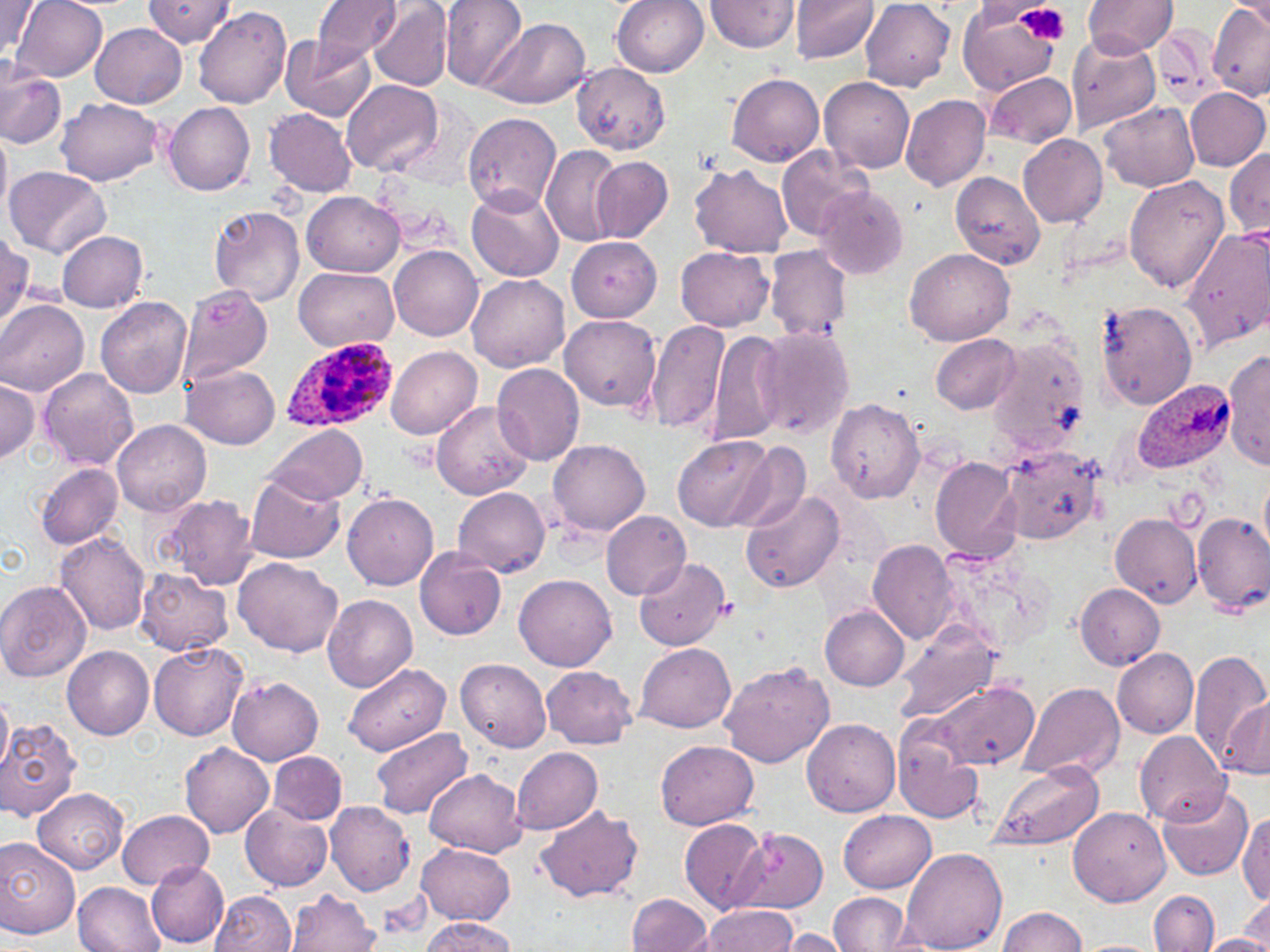

Summary:
  - Coordinate format: approximate bounding boxes as named x1/y1/x2/y2 corners in pixels
  - Uninfected red blood cell locations: (x1=12, y1=0, x2=108, y2=82), (x1=144, y1=0, x2=236, y2=46), (x1=312, y1=0, x2=403, y2=61), (x1=369, y1=0, x2=454, y2=92), (x1=441, y1=0, x2=529, y2=92), (x1=613, y1=0, x2=709, y2=77), (x1=705, y1=0, x2=799, y2=55), (x1=789, y1=0, x2=879, y2=65), (x1=1083, y1=1, x2=1176, y2=57), (x1=860, y1=2, x2=954, y2=90), (x1=1, y1=3, x2=40, y2=60), (x1=1207, y1=4, x2=1270, y2=100), (x1=958, y1=5, x2=1062, y2=95), (x1=194, y1=7, x2=292, y2=108), (x1=482, y1=18, x2=591, y2=109), (x1=90, y1=23, x2=186, y2=108), (x1=1154, y1=27, x2=1223, y2=106), (x1=280, y1=34, x2=377, y2=121), (x1=1068, y1=34, x2=1160, y2=131), (x1=572, y1=63, x2=670, y2=153), (x1=0, y1=69, x2=67, y2=150), (x1=984, y1=72, x2=1077, y2=147), (x1=725, y1=73, x2=824, y2=166), (x1=819, y1=77, x2=914, y2=173), (x1=342, y1=79, x2=444, y2=176), (x1=1185, y1=87, x2=1269, y2=171), (x1=900, y1=92, x2=990, y2=191), (x1=56, y1=98, x2=163, y2=186), (x1=162, y1=102, x2=256, y2=197), (x1=1100, y1=102, x2=1199, y2=193), (x1=265, y1=109, x2=358, y2=196), (x1=461, y1=111, x2=563, y2=214), (x1=0, y1=125, x2=11, y2=224), (x1=1017, y1=132, x2=1107, y2=227), (x1=541, y1=146, x2=626, y2=246), (x1=777, y1=146, x2=872, y2=242), (x1=1224, y1=151, x2=1270, y2=236), (x1=590, y1=156, x2=674, y2=242), (x1=691, y1=164, x2=793, y2=258), (x1=4, y1=166, x2=111, y2=259), (x1=950, y1=172, x2=1045, y2=269), (x1=1124, y1=173, x2=1229, y2=292), (x1=468, y1=184, x2=565, y2=280), (x1=815, y1=187, x2=909, y2=279), (x1=303, y1=191, x2=403, y2=277), (x1=207, y1=204, x2=306, y2=307), (x1=1178, y1=225, x2=1270, y2=354), (x1=0, y1=231, x2=32, y2=324), (x1=57, y1=231, x2=148, y2=311), (x1=567, y1=236, x2=661, y2=322), (x1=391, y1=245, x2=484, y2=340), (x1=904, y1=246, x2=1016, y2=345), (x1=765, y1=247, x2=851, y2=341), (x1=676, y1=248, x2=774, y2=332), (x1=293, y1=267, x2=399, y2=350), (x1=467, y1=274, x2=568, y2=371), (x1=177, y1=281, x2=273, y2=385), (x1=95, y1=297, x2=192, y2=399), (x1=0, y1=300, x2=89, y2=396), (x1=1096, y1=300, x2=1198, y2=411), (x1=560, y1=313, x2=660, y2=411), (x1=648, y1=319, x2=730, y2=436), (x1=708, y1=327, x2=786, y2=449), (x1=755, y1=327, x2=854, y2=440), (x1=931, y1=334, x2=1021, y2=414), (x1=972, y1=344, x2=1084, y2=452), (x1=388, y1=346, x2=481, y2=439), (x1=1224, y1=349, x2=1270, y2=471), (x1=492, y1=363, x2=587, y2=468), (x1=182, y1=364, x2=280, y2=449), (x1=37, y1=368, x2=138, y2=471), (x1=0, y1=378, x2=42, y2=464), (x1=825, y1=398, x2=926, y2=504), (x1=432, y1=400, x2=533, y2=500), (x1=113, y1=421, x2=210, y2=517), (x1=266, y1=424, x2=365, y2=505), (x1=673, y1=436, x2=774, y2=530), (x1=547, y1=439, x2=651, y2=536), (x1=729, y1=443, x2=811, y2=534), (x1=998, y1=445, x2=1105, y2=544), (x1=930, y1=457, x2=1022, y2=562), (x1=34, y1=462, x2=123, y2=550), (x1=245, y1=473, x2=346, y2=564), (x1=1259, y1=474, x2=1270, y2=556), (x1=452, y1=487, x2=551, y2=578), (x1=740, y1=488, x2=847, y2=594), (x1=342, y1=493, x2=438, y2=591), (x1=159, y1=494, x2=260, y2=589), (x1=601, y1=509, x2=691, y2=598), (x1=1110, y1=511, x2=1201, y2=604), (x1=1192, y1=513, x2=1270, y2=615), (x1=55, y1=530, x2=150, y2=637), (x1=867, y1=539, x2=959, y2=645), (x1=414, y1=547, x2=507, y2=640), (x1=635, y1=557, x2=730, y2=652), (x1=233, y1=558, x2=343, y2=658), (x1=136, y1=569, x2=233, y2=655), (x1=514, y1=574, x2=618, y2=672), (x1=0, y1=581, x2=91, y2=682), (x1=1074, y1=584, x2=1164, y2=669), (x1=323, y1=594, x2=418, y2=690), (x1=819, y1=604, x2=909, y2=690), (x1=893, y1=620, x2=1004, y2=724), (x1=148, y1=642, x2=247, y2=739), (x1=636, y1=643, x2=736, y2=734), (x1=61, y1=645, x2=154, y2=740), (x1=1111, y1=648, x2=1198, y2=738), (x1=1188, y1=649, x2=1269, y2=775), (x1=457, y1=658, x2=552, y2=752), (x1=719, y1=662, x2=833, y2=768), (x1=345, y1=664, x2=451, y2=755), (x1=542, y1=666, x2=637, y2=748), (x1=228, y1=676, x2=324, y2=765), (x1=1018, y1=680, x2=1126, y2=782), (x1=933, y1=683, x2=1039, y2=771), (x1=0, y1=692, x2=13, y2=783), (x1=1221, y1=694, x2=1269, y2=779), (x1=802, y1=718, x2=901, y2=816), (x1=1, y1=719, x2=82, y2=822), (x1=372, y1=726, x2=472, y2=819), (x1=1134, y1=730, x2=1230, y2=827), (x1=892, y1=732, x2=984, y2=823), (x1=180, y1=740, x2=274, y2=837), (x1=655, y1=740, x2=757, y2=830), (x1=512, y1=747, x2=604, y2=835), (x1=267, y1=751, x2=346, y2=824), (x1=990, y1=762, x2=1104, y2=850), (x1=425, y1=769, x2=526, y2=859), (x1=1156, y1=784, x2=1253, y2=880), (x1=33, y1=788, x2=128, y2=874), (x1=325, y1=800, x2=416, y2=896), (x1=534, y1=804, x2=645, y2=903), (x1=240, y1=805, x2=332, y2=892), (x1=1067, y1=806, x2=1171, y2=907), (x1=118, y1=809, x2=213, y2=890), (x1=839, y1=810, x2=935, y2=892), (x1=1238, y1=813, x2=1270, y2=905), (x1=679, y1=818, x2=768, y2=913), (x1=736, y1=833, x2=829, y2=914), (x1=0, y1=840, x2=81, y2=938), (x1=416, y1=843, x2=515, y2=924), (x1=898, y1=847, x2=1008, y2=952), (x1=146, y1=858, x2=228, y2=947), (x1=75, y1=883, x2=162, y2=951), (x1=287, y1=889, x2=380, y2=952), (x1=210, y1=891, x2=296, y2=951), (x1=1149, y1=891, x2=1219, y2=952), (x1=828, y1=892, x2=910, y2=951), (x1=626, y1=894, x2=715, y2=951), (x1=1241, y1=894, x2=1270, y2=946), (x1=697, y1=903, x2=799, y2=952), (x1=997, y1=907, x2=1086, y2=952), (x1=421, y1=917, x2=517, y2=951), (x1=775, y1=928, x2=850, y2=951), (x1=1202, y1=934, x2=1270, y2=951), (x1=1069, y1=940, x2=1164, y2=952)
  - Platelet locations: (x1=1014, y1=3, x2=1069, y2=45), (x1=716, y1=596, x2=738, y2=621)
  - Plasmodium ovale-infected red blood cell locations: (x1=282, y1=335, x2=397, y2=437), (x1=1131, y1=379, x2=1237, y2=473)
  - Slide-level diagnosis: Plasmodium ovale
  - Stain: May-Grünwald-Giemsa
  - Image size: 1270×952 pixels
  - Field of view: one of a larger specimen
  - Magnification: 1000x
  - Modality: light microscopy
  - Preparation: thin blood film